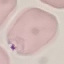
malaria_status: parasitized
preparation: thin smear
stain: Giemsa
capture: smartphone camera at the microscope eyepiece
image_type: automatically extracted cell patch, resized to 64 × 64 pixels